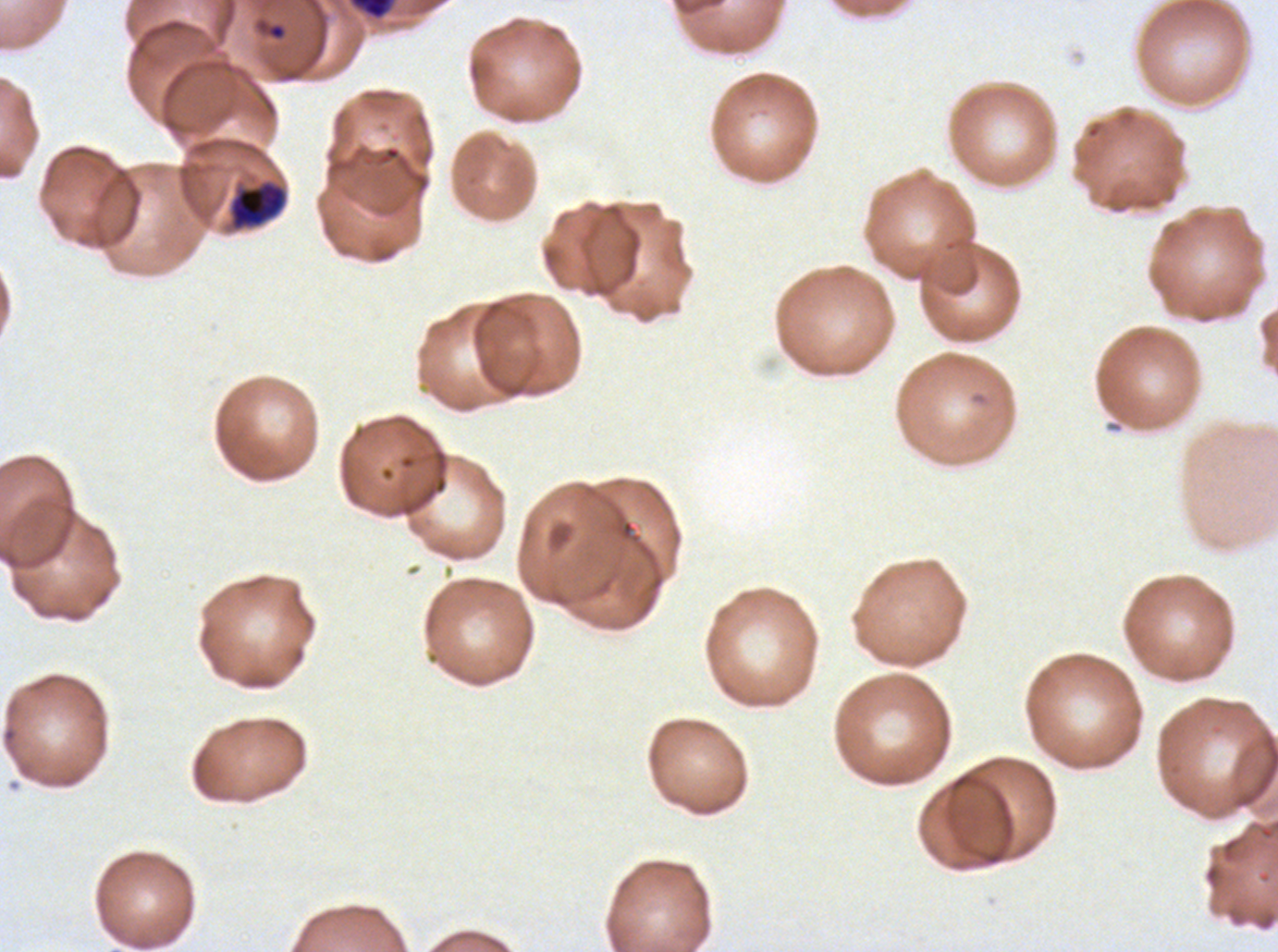 Approximate bounding rectangles given as corner coordinates in pixels from the top-left. Early schizont locations: (x1=229, y1=181, x2=285, y2=228). Ring locations: (x1=253, y1=17, x2=289, y2=43). Debris locations: (x1=349, y1=0, x2=395, y2=20). Ex-vivo Plasmodium falciparum culture from a patient in The Gambia, grown for 24 to 48 hours. Image is 1278×952 pixels. Thin blood film. Life-cycle stages observed: ring, early schizont. A sub-image separated from a larger composite. Giemsa-stained preparation.